Assess for malaria.
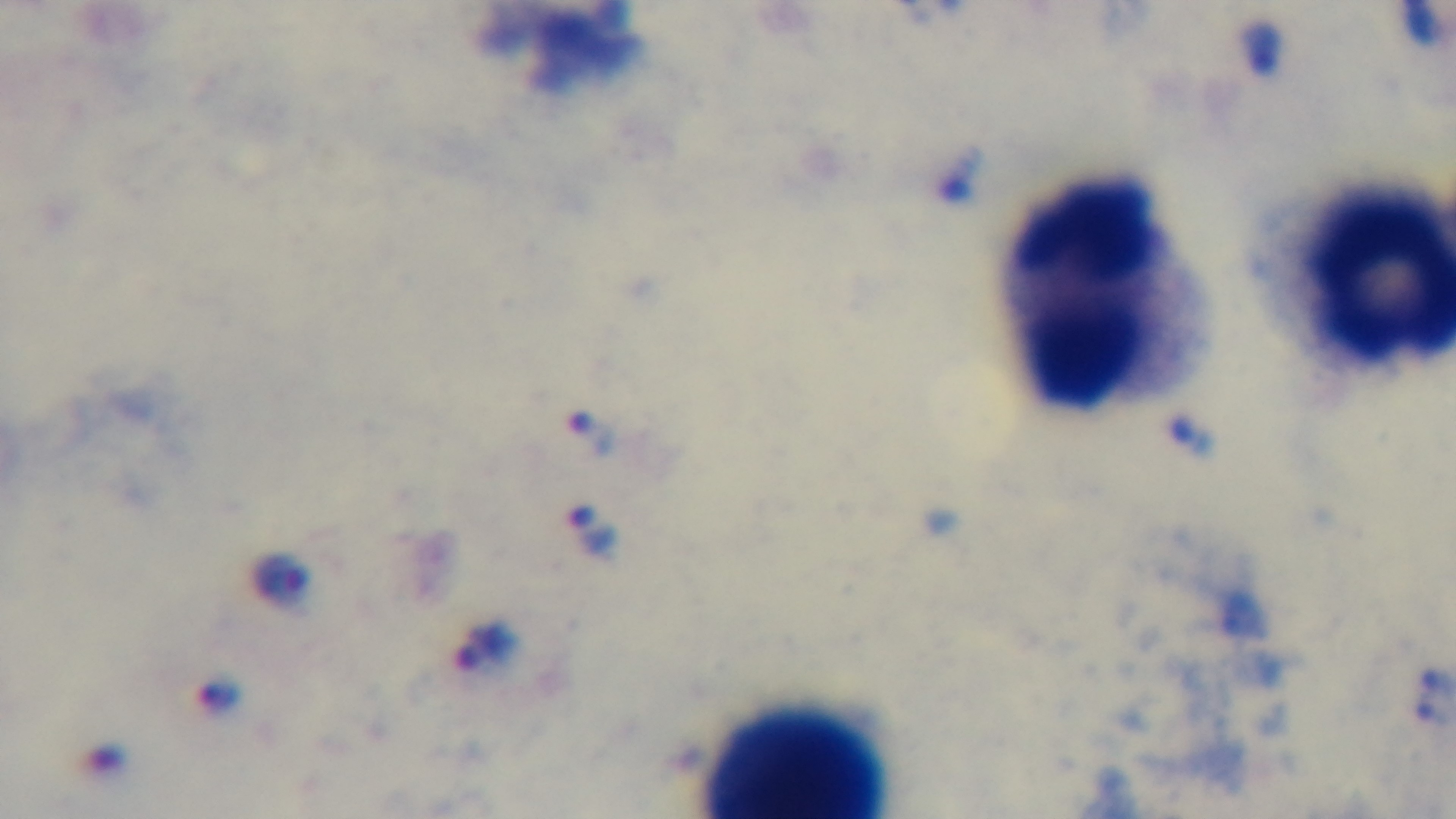

Positive.

Summary:
  - Capture: mounted 4K digital camera
  - Stain: Giemsa
  - Field of view: one from the slide
  - Objective: 100x oil immersion
  - Preparation: thick smear
  - Modality: light microscopy